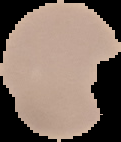
Image is 121×142 pixels. Segmented cell region on a black background. Result: Plasmodium parasites identified. From a thin blood smear.